State which parasite is depicted.
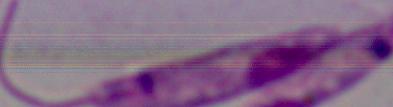
This is Leishmania.

Photomicrograph. 1000x magnification.